State which parasite is depicted.
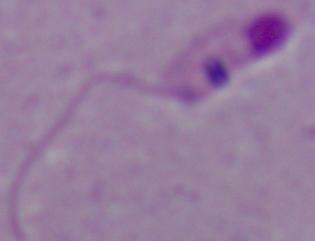

This is Leishmania.

Micrograph. 1000x magnification.